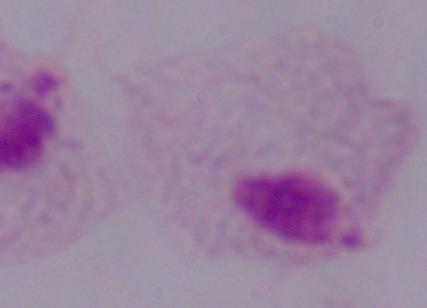
Photomicrograph. A trichomonad is shown. 1000x magnification.